Classify this cell by malaria status.
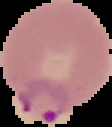
It is parasitized.

Segmented cell region on a black background. Image is 112×127 pixels. From a thin blood smear.